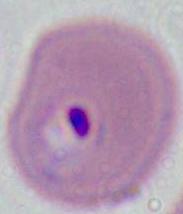 Captured at either 400x or 1000x magnification. A Plasmodium parasite is shown. Micrograph.